State the blood parasite species.
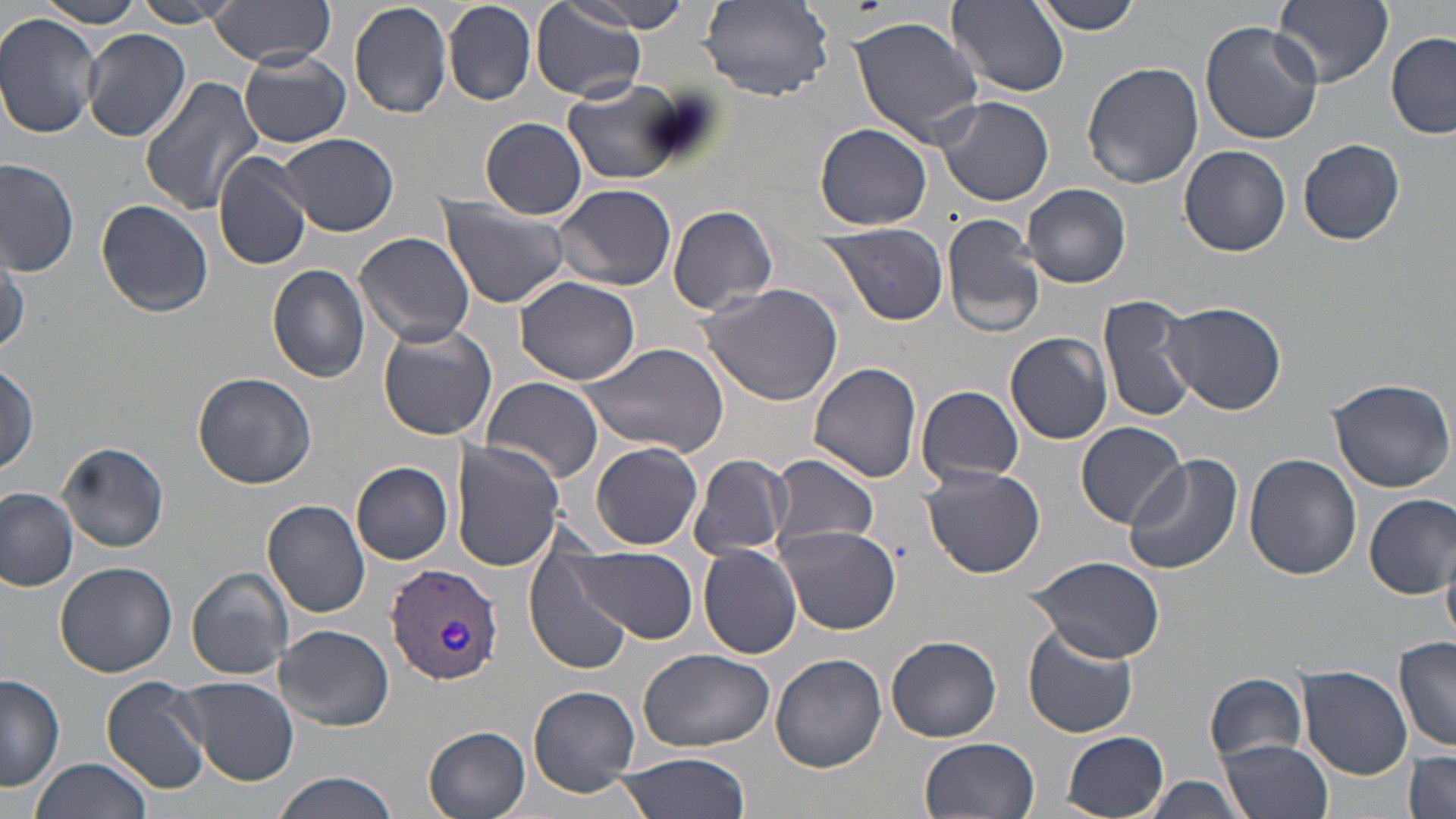

Plasmodium vivax.

magnification = 1000x
image size = 1456×819 pixels
uninfected red blood cell locations = approximate bounding boxes as (x1,y1)-(x2,y2) corner pairs in pixels: (35,0)-(148,26), (209,0)-(336,64), (349,0)-(454,118), (1030,0)-(1145,34), (1272,0)-(1392,88), (132,1)-(233,27), (444,1)-(535,105), (569,1)-(699,34), (700,1)-(836,103), (949,1)-(1068,95), (530,6)-(648,102), (0,14)-(102,137), (851,14)-(989,144), (1201,21)-(1322,143), (82,28)-(191,142), (1385,33)-(1456,139), (98,49)-(239,182), (239,52)-(351,147), (1082,60)-(1201,189), (139,76)-(263,214), (564,81)-(689,185), (937,97)-(1054,207), (482,117)-(588,218), (816,123)-(930,232), (280,132)-(398,235), (1298,139)-(1405,245), (1179,145)-(1291,256), (213,152)-(314,272), (0,157)-(79,276), (555,183)-(678,291), (1024,183)-(1131,288), (437,197)-(571,309), (95,199)-(214,317), (667,204)-(778,316), (942,212)-(1047,338), (818,222)-(948,326), (353,231)-(475,349), (0,248)-(28,360), (266,264)-(372,384), (515,276)-(640,386), (701,279)-(844,406), (1098,294)-(1198,424), (1163,302)-(1284,414), (377,325)-(496,442), (1005,332)-(1114,444), (578,341)-(731,459), (0,360)-(40,475), (809,360)-(922,484), (193,372)-(317,490), (481,376)-(603,486), (1327,377)-(1454,492), (916,385)-(1025,485), (1076,422)-(1187,530), (59,440)-(169,552), (451,440)-(565,570), (591,441)-(703,550), (768,452)-(879,555), (688,453)-(793,561), (1244,453)-(1361,580), (1123,455)-(1243,577), (351,461)-(454,565), (922,467)-(1045,579), (0,488)-(79,593), (1364,495)-(1455,596), (264,499)-(371,618), (776,524)-(901,635), (699,544)-(803,659), (568,546)-(698,645), (1027,556)-(1168,663), (527,557)-(632,674), (56,561)-(175,676), (186,568)-(294,680), (276,625)-(395,729), (1023,625)-(1138,738), (887,635)-(1001,743), (1395,637)-(1456,754), (639,649)-(774,752), (771,653)-(886,772), (1299,666)-(1413,781), (1205,672)-(1307,762), (0,673)-(66,792), (101,675)-(211,796), (177,676)-(300,784), (526,685)-(641,796), (424,726)-(531,819), (1064,731)-(1169,816), (920,736)-(1040,819), (1219,738)-(1333,819), (1404,750)-(1456,819), (615,751)-(750,819), (34,756)-(154,819), (272,772)-(401,819), (1138,775)-(1254,817)
Plasmodium vivax-infected red blood cell locations = approximate bounding boxes as (x1,y1)-(x2,y2) corner pairs in pixels: (385,562)-(502,685)
preparation = thin blood smear
stain = May-Grünwald-Giemsa
field of view = one of a larger specimen
modality = light microscopy